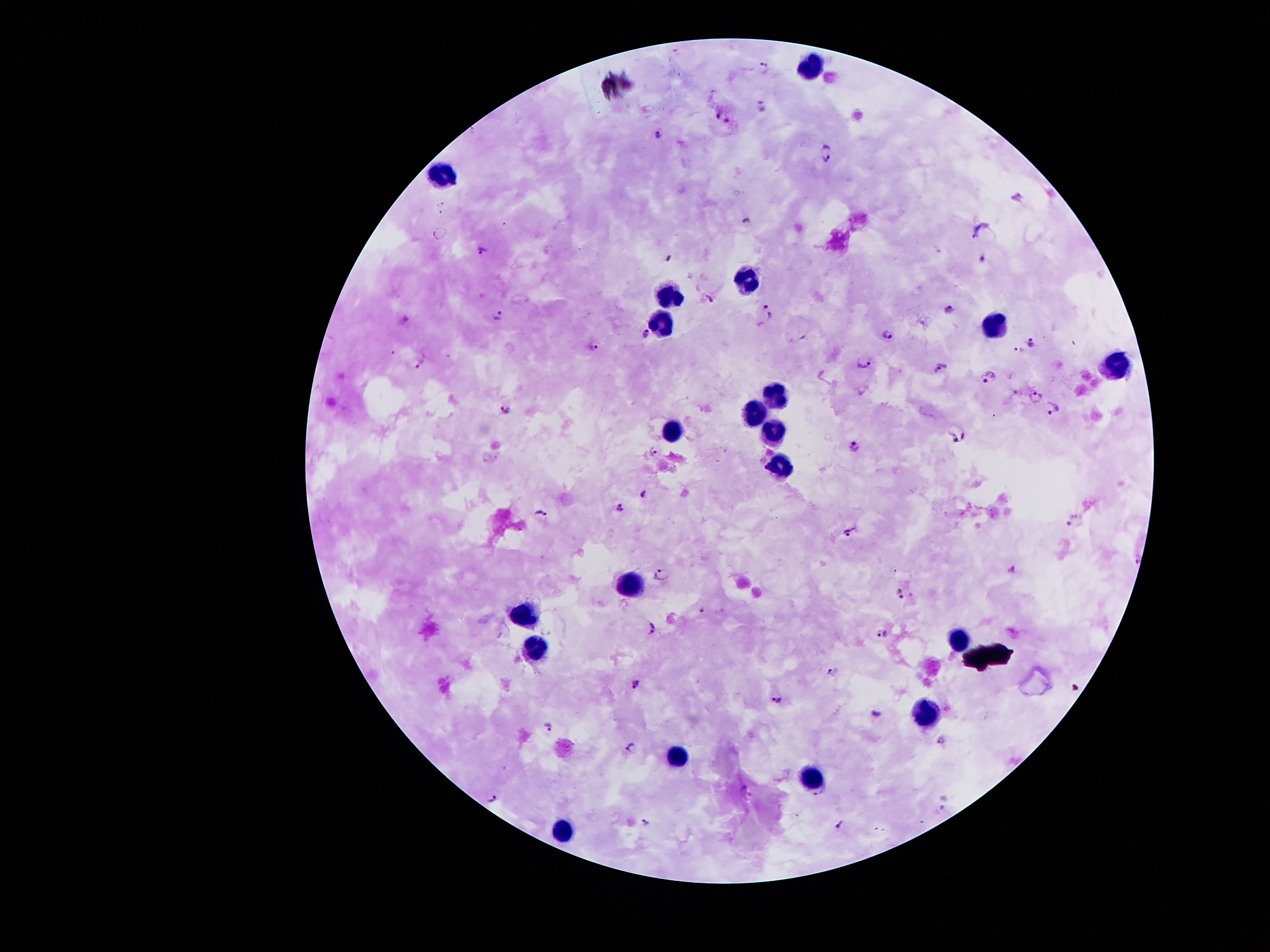

Approximate centers as {x, y} in pixels. Malaria parasite locations: {762, 67}, {762, 106}, {717, 115}, {727, 120}, {657, 130}, {826, 154}, {1014, 200}, {746, 220}, {978, 231}, {481, 250}, {981, 256}, {707, 299}, {949, 309}, {768, 311}, {497, 315}, {646, 331}, {888, 331}, {1033, 339}, {592, 349}, {1017, 349}, {863, 362}, {420, 364}, {940, 367}, {990, 373}, {1015, 392}, {1034, 396}, {1050, 408}, {506, 409}, {956, 432}, {852, 446}, {654, 452}, {643, 493}, {620, 507}, {540, 513}, {1072, 520}, {847, 530}, {1138, 556}, {1013, 569}, {662, 573}, {900, 594}, {653, 628}, {882, 633}, {830, 671}, {636, 684}, {777, 698}, {878, 714}, {549, 725}, {943, 739}, {631, 746}, {747, 790}, {493, 798}, {646, 822}, {840, 824}. Leukocyte locations: {809, 64}, {443, 175}, {749, 276}, {667, 297}, {660, 315}, {992, 327}, {1113, 362}, {774, 394}, {755, 413}, {774, 429}, {672, 431}, {782, 466}, {622, 583}, {527, 611}, {961, 637}, {536, 645}, {926, 711}, {677, 756}, {810, 780}, {561, 832}. Giemsa stain. Thick peripheral-blood smear. Patient malaria status: infected with Plasmodium falciparum. Single field of view. Image is 1270×952 pixels. 100x magnification. Smartphone photograph taken through the microscope eyepiece.